Assess the morphology of the erythrocytes.
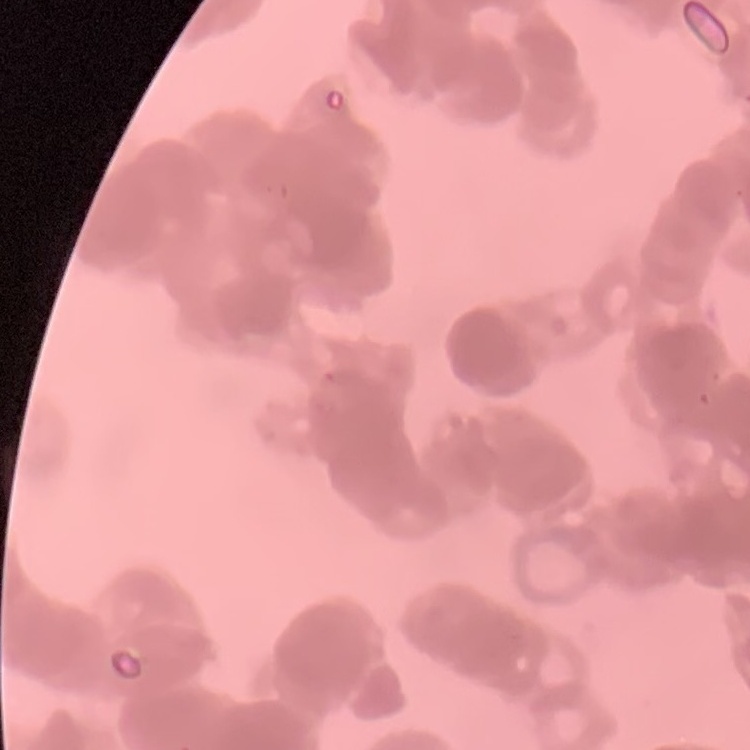
They show rouleaux formation.

Summary:
  - Stain: Field's or Giemsa
  - Image type: square crop of a larger photomicrograph
  - Preparation: thin blood film